Give the preparation type.
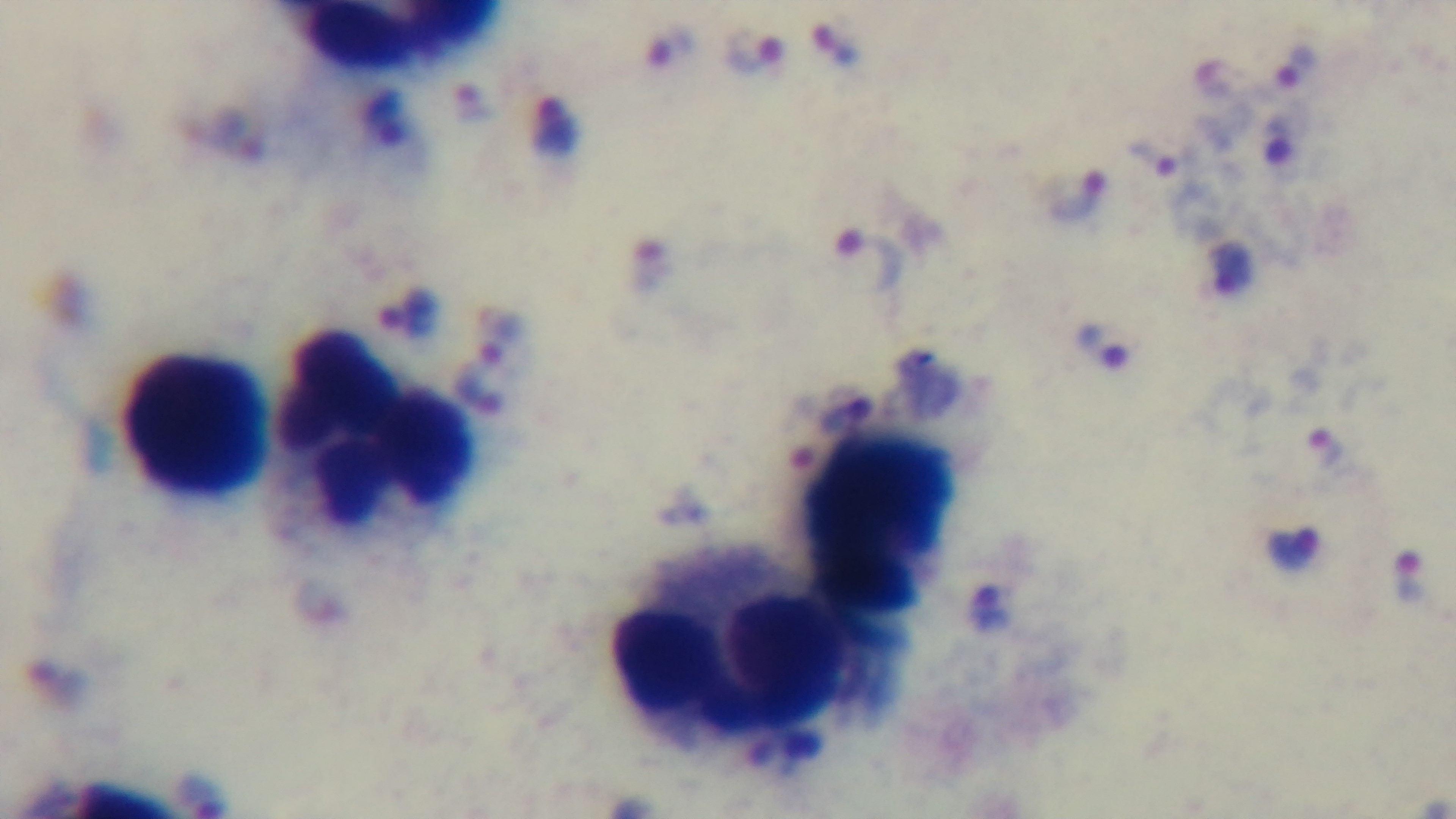
Thick.

Summary:
  - Stain: Giemsa
  - Field of view: single
  - Malaria status: infected
  - Capture: mounted 4K digital camera
  - Modality: light microscopy
  - Objective: 100x oil immersion